Report the malaria status of this cell.
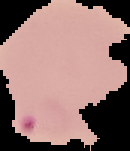

Parasitized.

{
  "image_type": "segmented cell region with the area outside set to black",
  "preparation": "thin blood film",
  "image_size": "130×151 pixels"
}